Comment on the morphology of the erythrocytes.
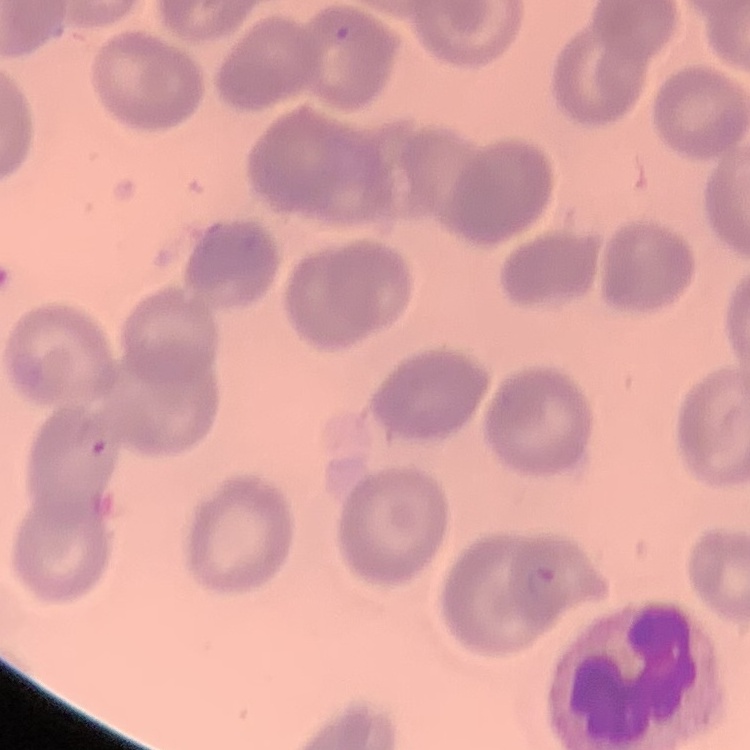
No rouleaux formation.

image type = one tile cut from a larger photomicrograph
stain = Field's or Giemsa
preparation = thin peripheral smear